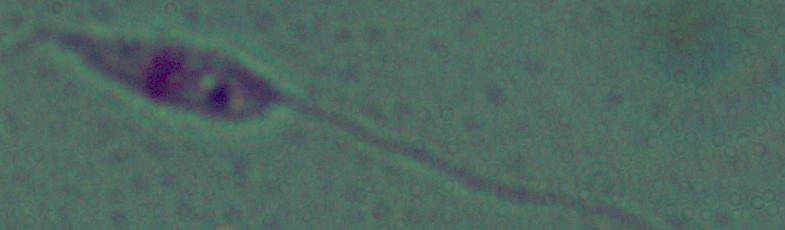
Photomicrograph. A Leishmania parasite is shown. 1000x magnification.